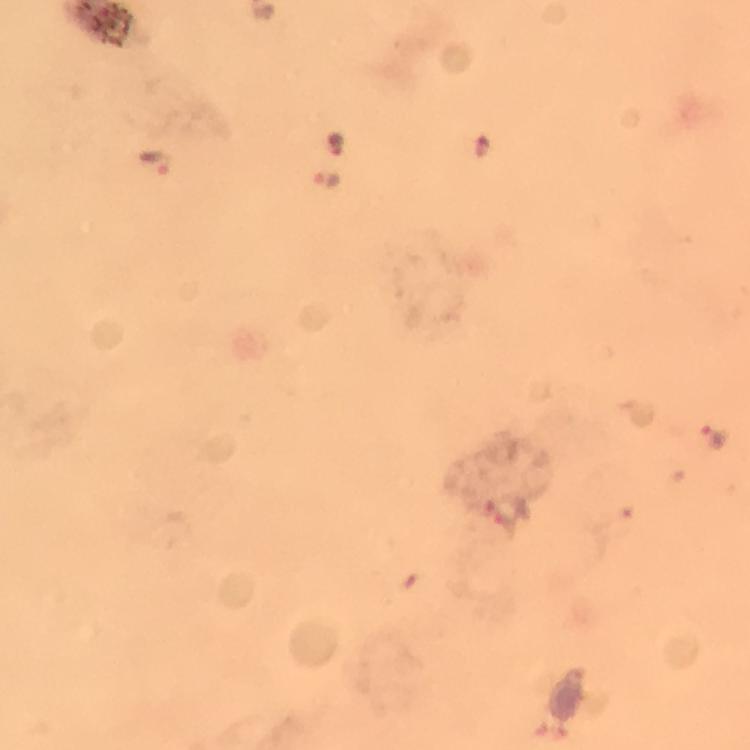
{
  "context": "from a malaria diagnostic workup",
  "image_size": "750×750 pixels",
  "cropped_from": "one field of view",
  "capture": "smartphone photograph through a microscope",
  "immersion_oil": "used",
  "plasmodium_parasite_locations": "approximate centers as {x, y} in pixels: {336, 144}, {158, 162}, {328, 179}, {719, 438}",
  "preparation": "thick blood film",
  "magnification": "100x",
  "stain": "Giemsa"
}